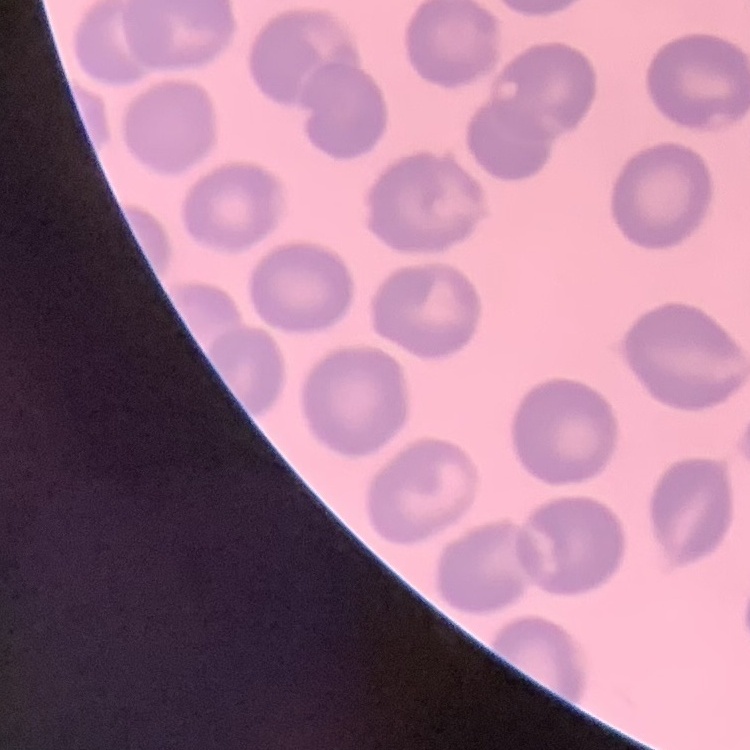

Summary:
  - Erythrocyte morphology: no rouleaux formation
  - Image type: square crop of a larger photomicrograph
  - Stain: Field's or Giemsa
  - Preparation: thin blood film